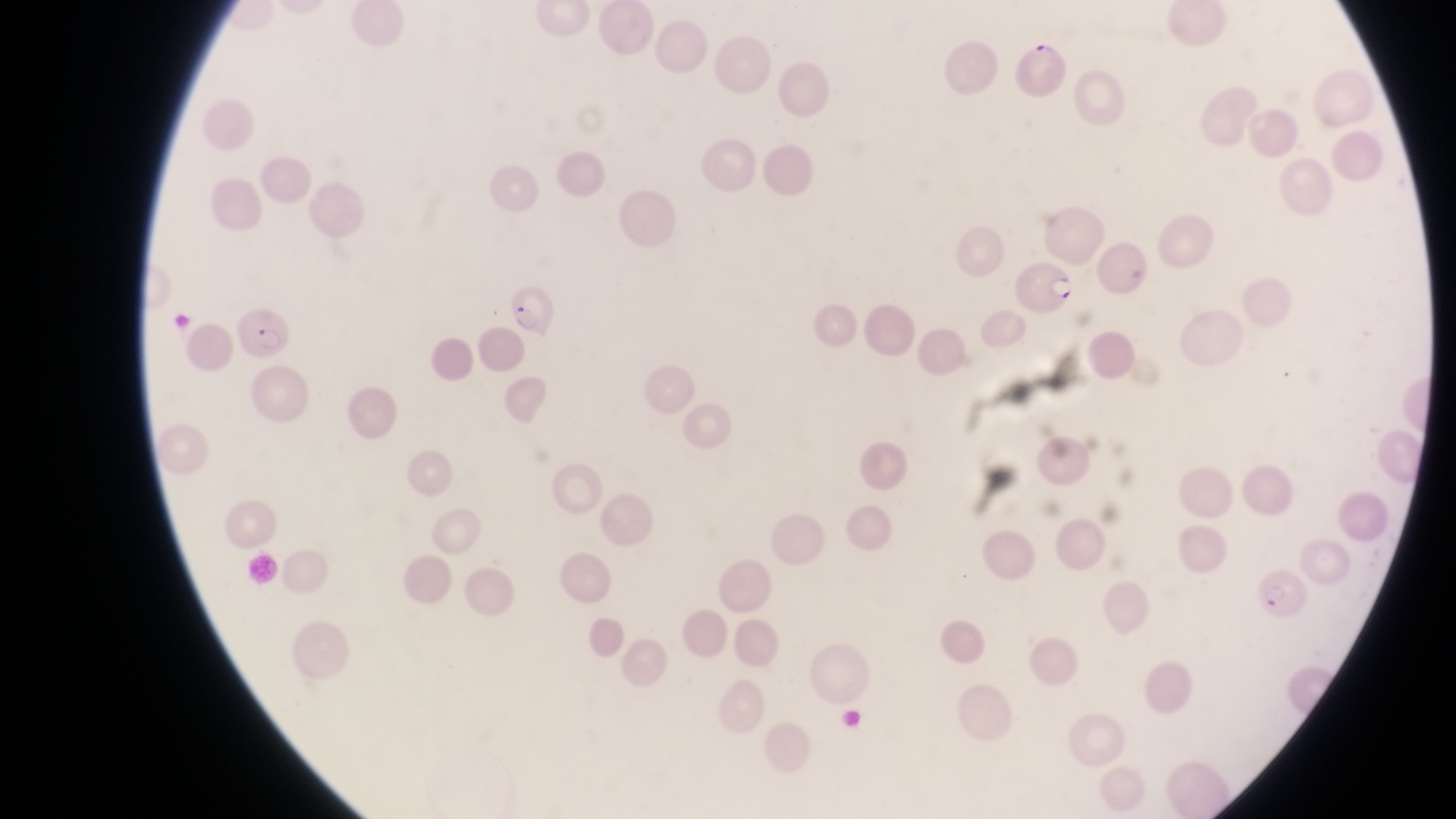

Approximate bounding boxes as left top right bottom in pixels. Artifact (platelet-like body, stain precipitate, or debris) locations: 1034 36 1061 60. Parasitised red blood cell locations: 1009 265 1078 314; 508 278 558 339; 238 309 293 365; 1254 573 1309 625. Sample from Uganda. Thin blood film. Single field of view. Photographed through the eyepiece of an Olympus CX-23 microscope with a smartphone camera. Magnification of 1000x. Image is 1456×819 pixels.